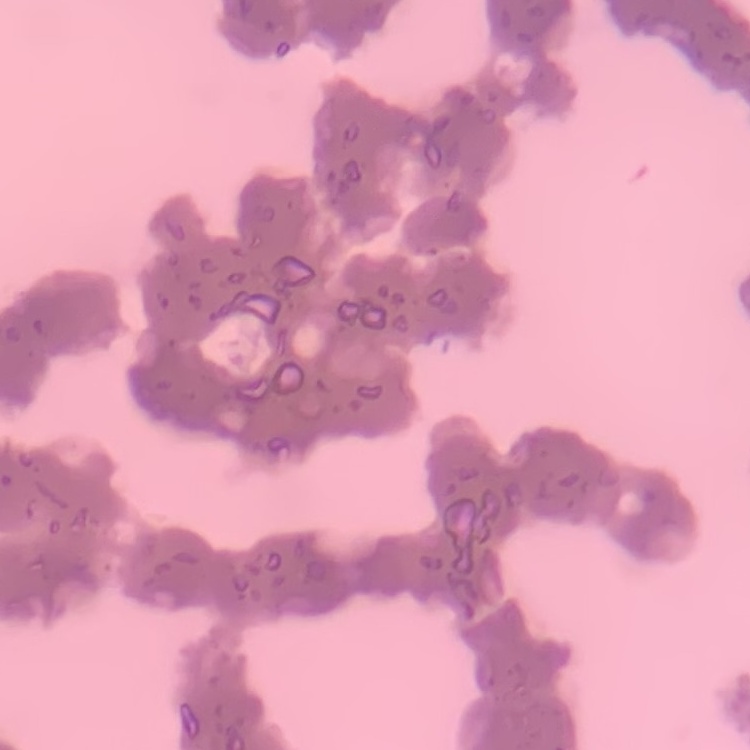

red blood cell morphology = rouleaux formation
image type = one tile cut from a larger photomicrograph
preparation = thin blood film
stain = Field's or Giemsa